Classify this cell by malaria status.
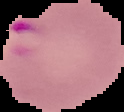

Parasitized.

preparation: thin blood smear
image_size: 124×112 pixels
image_type: segmented cell region on a black background